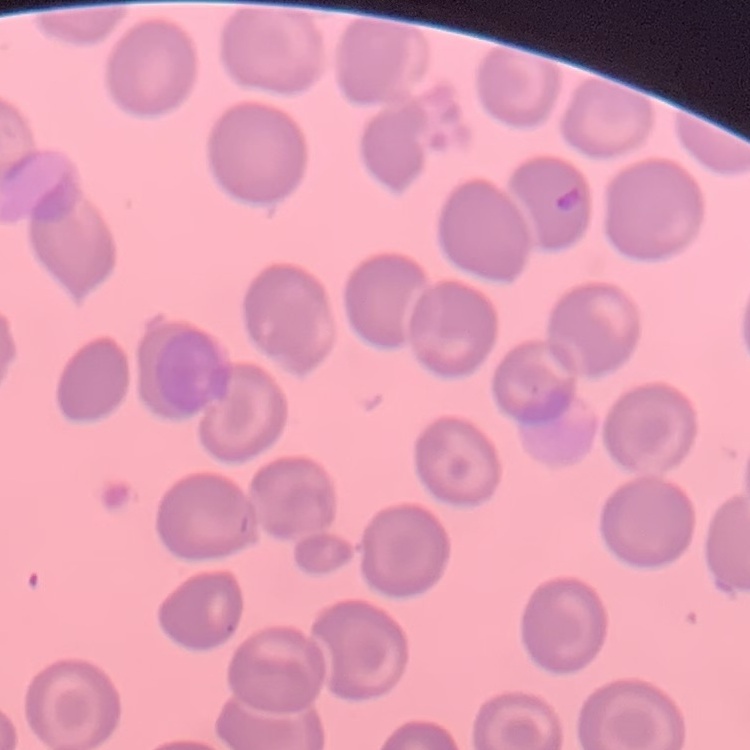
erythrocyte morphology = no rouleaux formation
image type = square crop of a larger photomicrograph
stain = Field's or Giemsa
preparation = thin peripheral smear